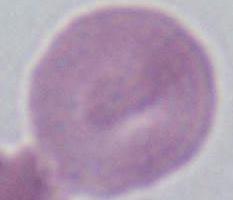

1000x magnification. Micrograph. A red blood cell is shown.